Outline each blood parasite and name the species.
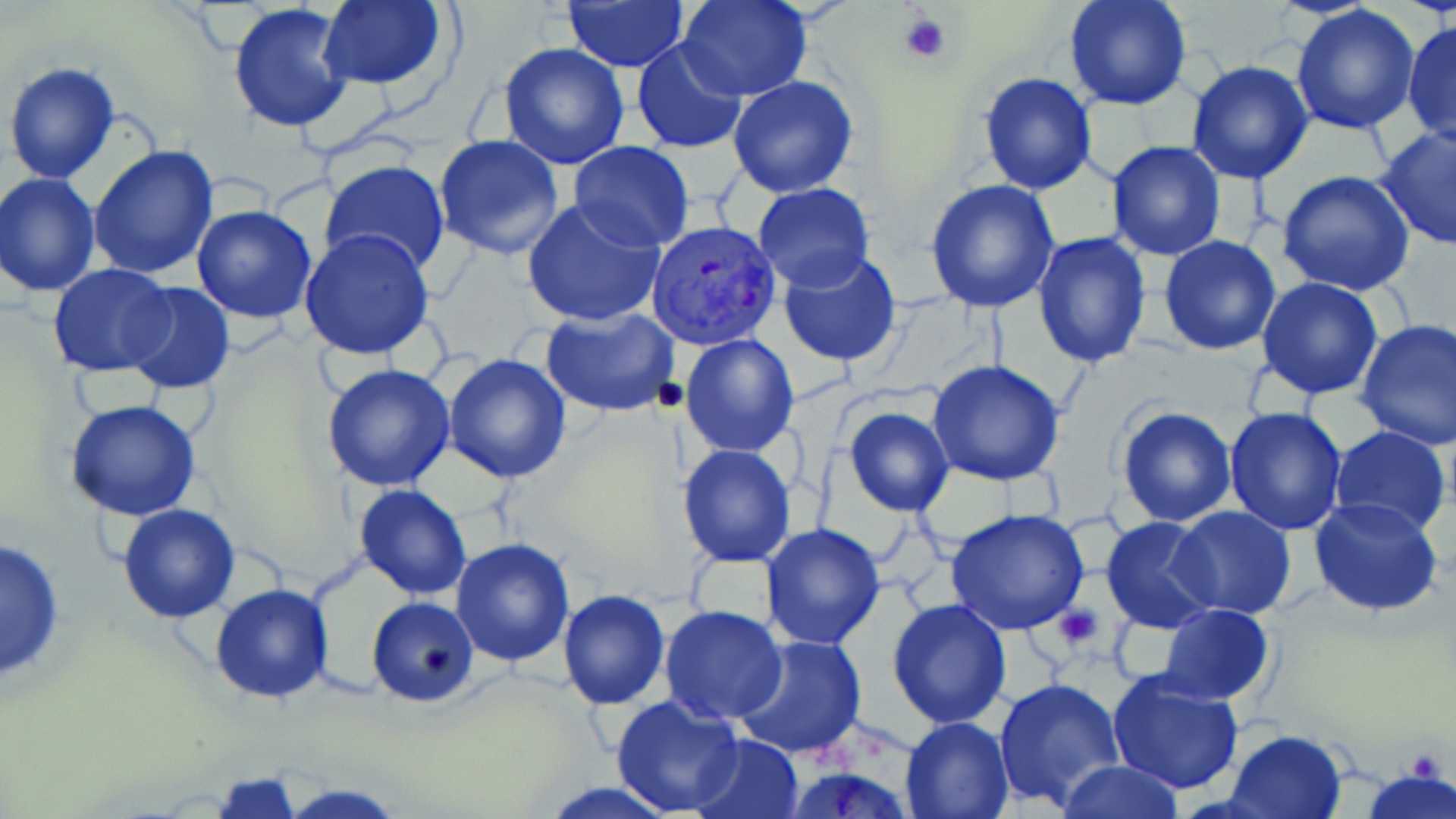
Approximate bounding boxes as (x1, y1, x2, y2) in pixels.
Plasmodium vivax-infected red blood cells: (647, 220, 784, 351).
No Plasmodium falciparum, Plasmodium ovale, Plasmodium malariae, Babesia divergens, or Trypanosoma brucei observed.

slide-level diagnosis = Plasmodium vivax
platelet locations = approximate bounding boxes as (x1, y1, x2, y2) in pixels: (896, 10, 951, 65), (1052, 602, 1103, 650)
modality = optical microscopy
uninfected red blood cell locations = approximate bounding boxes as (x1, y1, x2, y2) in pixels: (316, 0, 450, 91), (563, 0, 689, 72), (1062, 0, 1193, 112), (227, 1, 356, 135), (678, 1, 812, 101), (1290, 6, 1421, 134), (1403, 17, 1456, 147), (630, 38, 749, 155), (499, 42, 630, 170), (2, 58, 120, 185), (1186, 60, 1315, 185), (978, 71, 1097, 196), (727, 76, 859, 199), (1373, 127, 1456, 251), (434, 135, 565, 260), (1108, 141, 1225, 260), (569, 142, 694, 251), (89, 146, 219, 282), (320, 161, 450, 278), (1276, 170, 1418, 296), (1, 172, 101, 295), (924, 180, 1061, 315), (752, 183, 873, 292), (521, 198, 665, 328), (190, 203, 318, 324), (300, 229, 434, 360), (1031, 231, 1152, 366), (1158, 235, 1284, 355), (776, 250, 901, 368), (48, 262, 175, 377), (1257, 278, 1384, 401), (122, 283, 235, 395), (540, 305, 680, 419), (1355, 317, 1456, 453), (679, 334, 798, 457), (442, 354, 571, 483), (928, 361, 1065, 485), (321, 364, 455, 492), (64, 398, 201, 523), (1116, 406, 1237, 528), (843, 407, 954, 517), (1223, 408, 1347, 536), (1329, 424, 1453, 537), (677, 444, 795, 567), (355, 484, 472, 600), (1308, 496, 1444, 620), (117, 504, 238, 622), (1168, 506, 1296, 618), (945, 508, 1089, 635), (1101, 516, 1221, 635), (761, 523, 887, 650), (0, 535, 66, 683), (451, 537, 576, 667), (211, 582, 334, 704), (557, 590, 670, 709), (367, 596, 479, 705), (886, 597, 1012, 729), (1157, 604, 1276, 703), (659, 605, 787, 725), (731, 634, 865, 758), (1107, 671, 1244, 793), (994, 676, 1127, 813), (609, 695, 743, 816), (899, 716, 1016, 819), (1223, 729, 1348, 819), (688, 732, 803, 817), (1053, 759, 1186, 818), (777, 763, 922, 819), (1361, 769, 1456, 819), (211, 773, 305, 818), (278, 781, 409, 818), (538, 782, 682, 818)
stain = May-Grünwald-Giemsa
image size = 1456×819 pixels
preparation = thin blood film
field of view = one of a larger specimen
magnification = 1000x